Locate and identify every blood parasite.
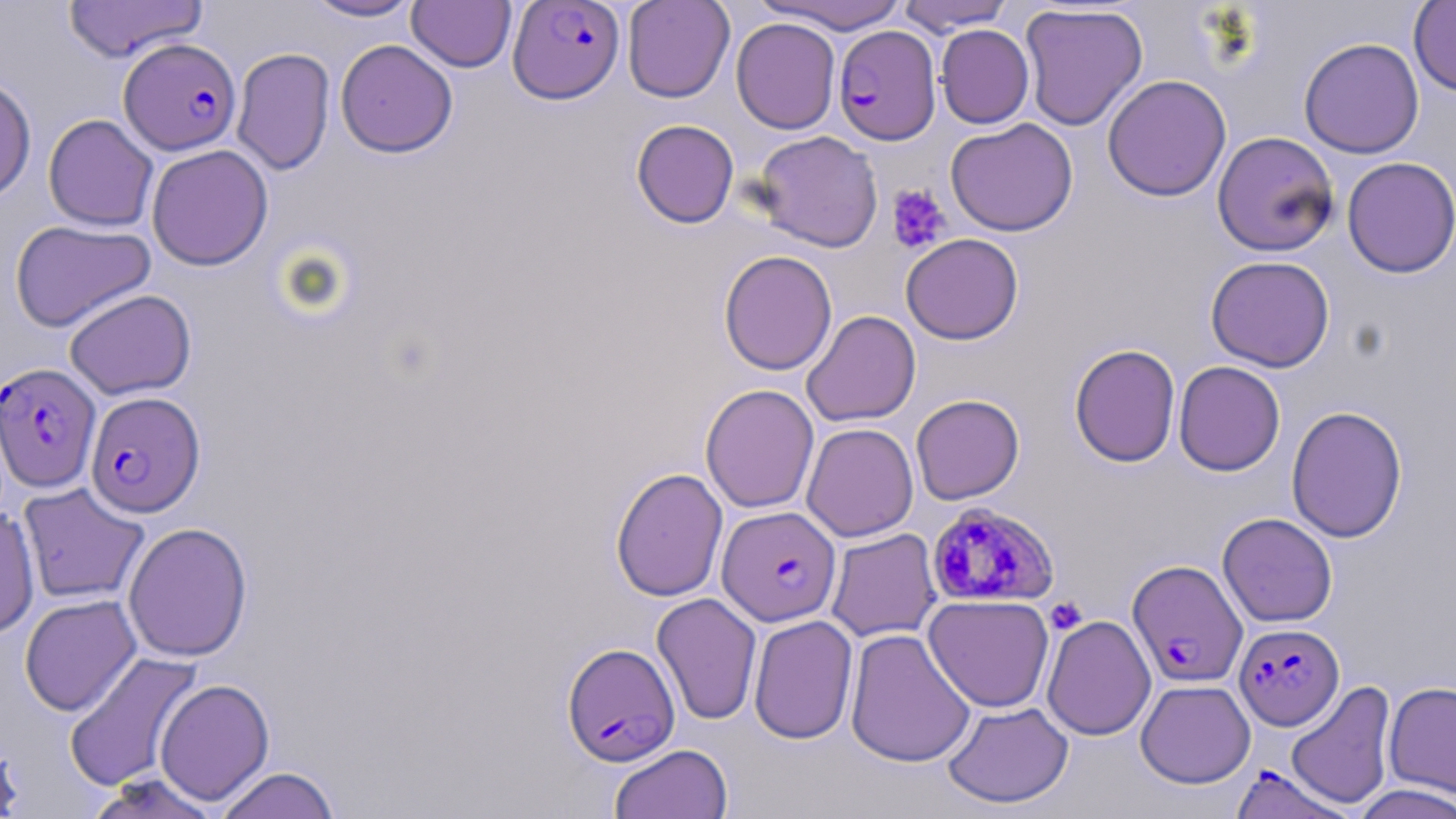
Approximate bounding boxes as (x1, y1, x2, y2) in pixels.
Plasmodium falciparum-infected red blood cells: (507, 0, 626, 104), (833, 25, 941, 145), (119, 37, 241, 155), (0, 362, 101, 492), (85, 391, 205, 518), (926, 501, 1059, 607), (717, 506, 841, 626), (1127, 559, 1248, 688), (1233, 623, 1344, 731), (561, 643, 681, 766), (1228, 763, 1357, 819).
No Plasmodium ovale, Plasmodium malariae, Plasmodium vivax, Babesia divergens, or Trypanosoma brucei observed.

Platelet locations: (886, 184, 951, 254), (1045, 597, 1087, 634). Uninfected red blood cell locations: (302, 0, 423, 22), (407, 0, 516, 73), (622, 0, 735, 103), (757, 0, 906, 34), (62, 1, 208, 63), (896, 1, 1015, 34), (1408, 1, 1456, 97), (1019, 4, 1148, 131), (731, 16, 841, 134), (935, 24, 1035, 129), (1298, 38, 1425, 159), (335, 39, 458, 158), (231, 47, 335, 176), (1102, 74, 1231, 202), (0, 75, 36, 203), (43, 114, 159, 232), (945, 118, 1078, 237), (631, 119, 739, 228), (753, 130, 884, 252), (1213, 131, 1340, 257), (146, 145, 274, 271), (1342, 156, 1456, 278), (9, 219, 156, 332), (901, 233, 1023, 344), (718, 249, 837, 376), (1205, 255, 1335, 372), (64, 289, 196, 399), (801, 310, 921, 427), (1069, 343, 1181, 468), (1173, 361, 1286, 477), (700, 383, 819, 513), (910, 394, 1025, 505), (1285, 405, 1408, 543), (801, 423, 919, 542), (610, 466, 728, 602), (17, 482, 150, 605), (0, 506, 40, 639), (1217, 512, 1338, 627), (123, 521, 253, 662), (825, 527, 942, 642), (651, 593, 762, 725), (19, 594, 141, 716), (923, 594, 1054, 712), (748, 614, 859, 745), (1041, 614, 1156, 741), (845, 628, 976, 769), (63, 651, 204, 792), (154, 678, 274, 805), (1135, 679, 1256, 788), (1285, 680, 1397, 810), (1384, 680, 1456, 798), (941, 701, 1074, 809), (1, 737, 25, 817), (609, 744, 733, 819), (214, 766, 341, 819), (87, 773, 222, 819), (1351, 783, 1456, 819). Slide-level diagnosis: Plasmodium falciparum. Single field of view. May-Grünwald-Giemsa stain. Light microscopy. Captured at 1000x magnification. Thin blood smear. Image is 1456×819 pixels.